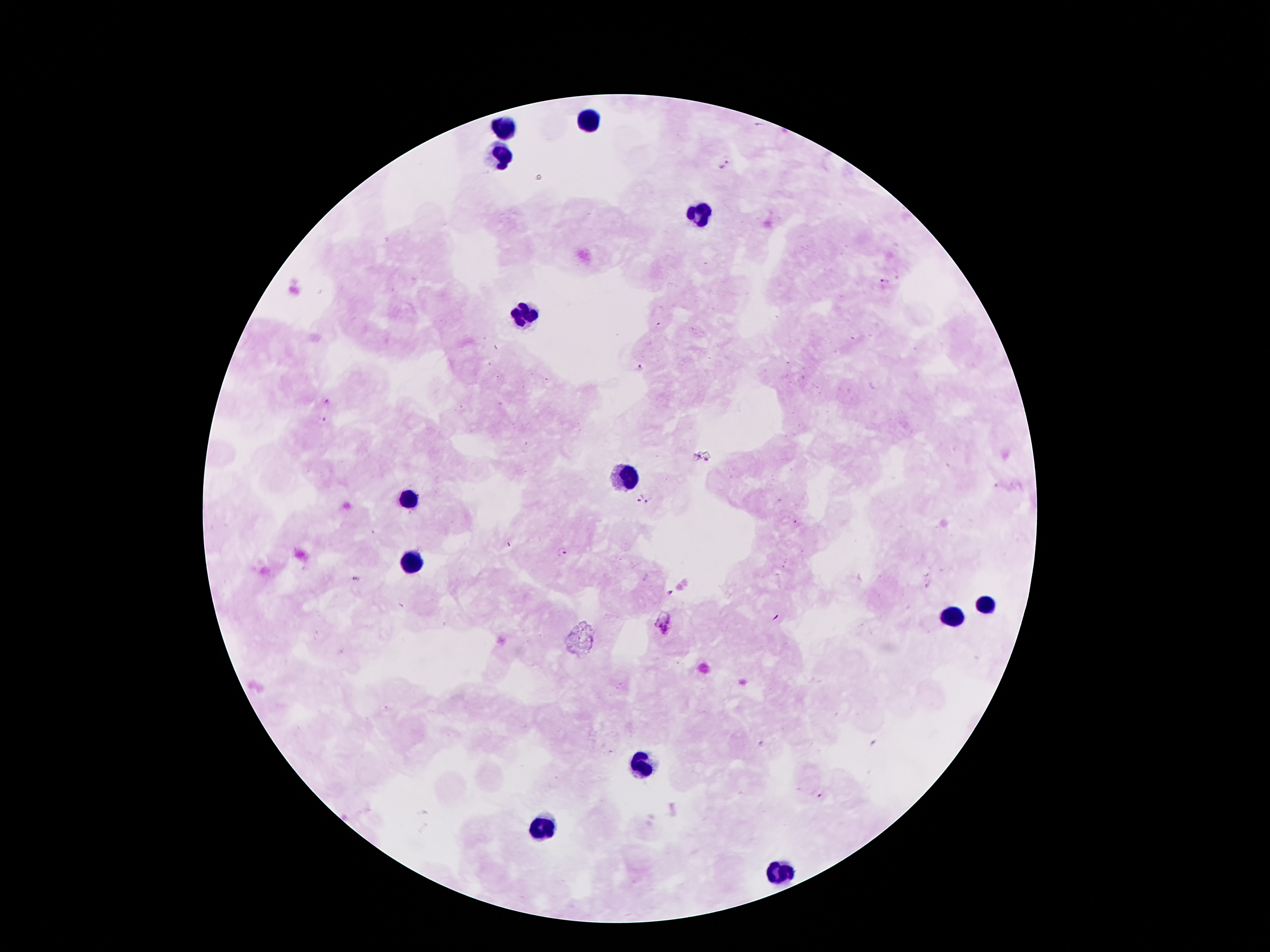 Approximate centers as {x, y} in pixels. Plasmodium parasite locations: {724, 165}, {882, 281}, {658, 325}, {638, 368}, {326, 402}, {322, 418}, {637, 496}, {649, 501}, {560, 552}, {672, 594}, {664, 627}, {818, 797}. Leukocyte locations: {590, 118}, {505, 129}, {503, 154}, {703, 211}, {524, 311}, {626, 479}, {412, 498}, {412, 559}, {987, 605}, {951, 618}, {644, 768}, {546, 827}, {783, 870}. Giemsa-stained preparation. Thick blood smear. Patient malaria status: positive for Plasmodium falciparum. Smartphone photograph taken through the microscope eyepiece. One field from this slide. Image is 1270×952 pixels. 100x magnification.